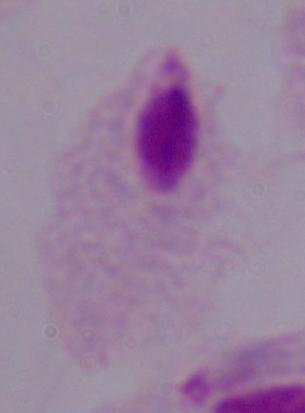

magnification = 1000x
modality = photomicrograph
identification = trichomonad